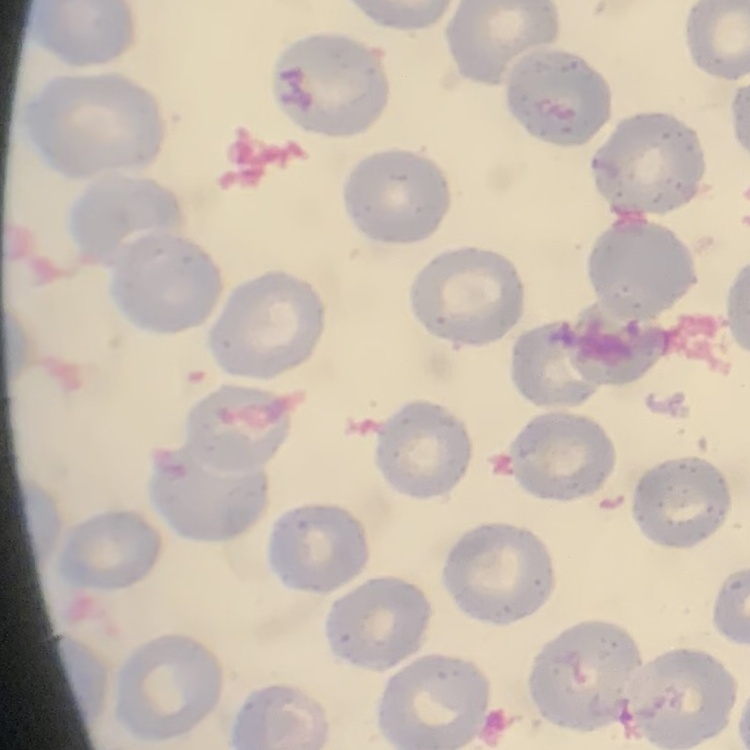

Summary:
  - Red blood cell morphology: no rouleaux formation
  - Preparation: thin peripheral smear
  - Image type: square crop of a larger photomicrograph
  - Stain: Field's or Giemsa